Identify the blood parasite species.
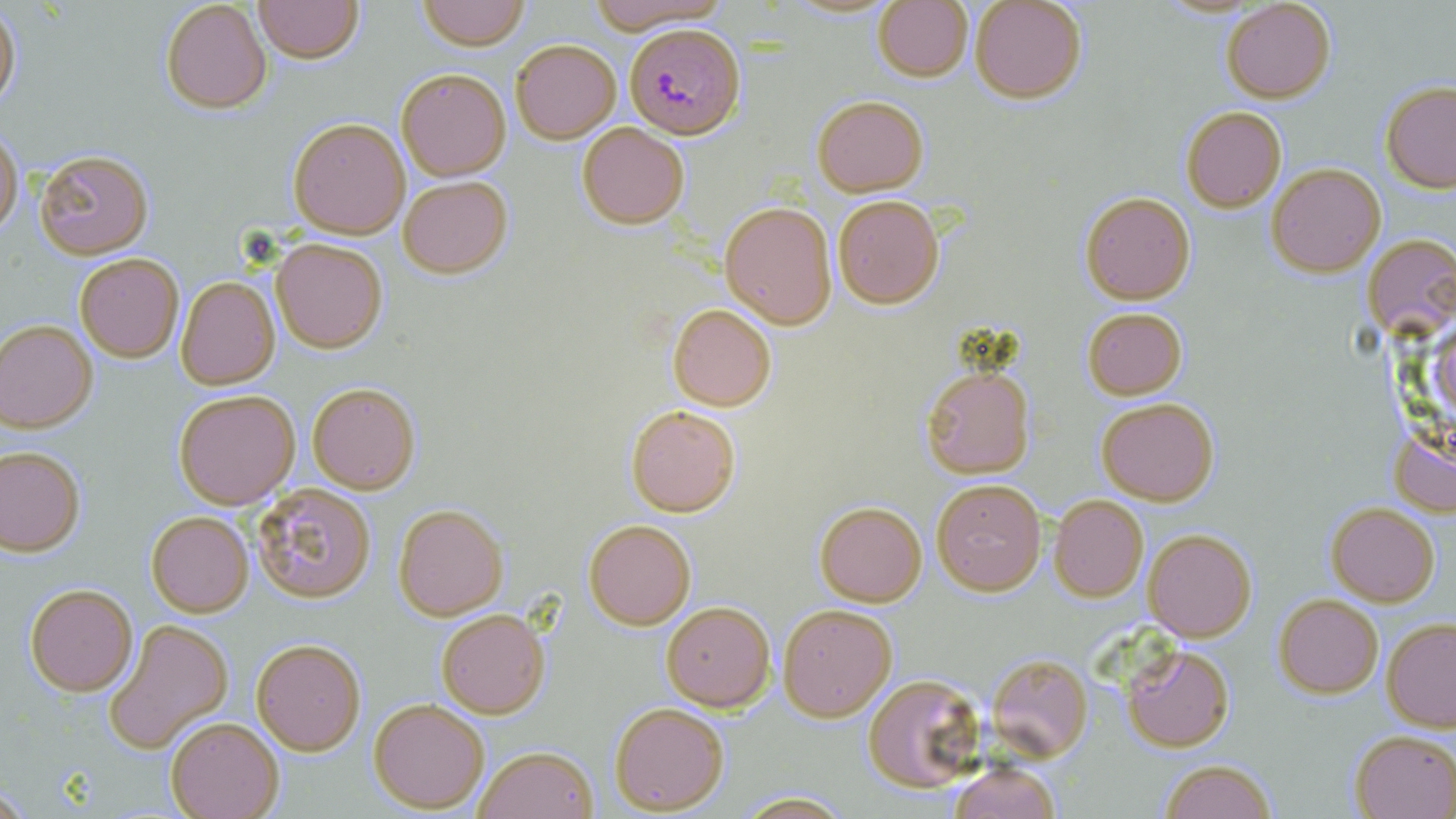
Plasmodium falciparum.

Approximate bounding boxes as (x1,y1)-(x2,y2) corner pairs in pixels. Uninfected red blood cell locations: (253,0)-(363,63), (417,0)-(528,50), (969,0)-(1088,105), (160,1)-(272,114), (582,1)-(731,31), (1220,1)-(1337,104), (872,2)-(974,82), (1,3)-(21,117), (511,39)-(621,144), (395,67)-(511,180), (1380,79)-(1456,193), (810,95)-(928,196), (1180,105)-(1286,213), (288,116)-(410,239), (576,122)-(689,229), (0,127)-(22,239), (33,148)-(155,260), (1267,163)-(1384,277), (397,176)-(512,278), (1079,190)-(1196,305), (834,195)-(944,309), (718,200)-(837,330), (1362,235)-(1454,339), (272,238)-(388,354), (73,253)-(185,363), (70,266)-(280,379), (175,275)-(281,390), (668,303)-(778,412), (1080,307)-(1187,401), (0,319)-(97,432), (920,364)-(1035,478), (307,382)-(421,495), (173,388)-(300,509), (1095,396)-(1220,507), (625,403)-(742,517), (1390,431)-(1456,517), (0,445)-(85,556), (932,478)-(1046,594), (253,482)-(378,603), (1049,495)-(1148,602), (813,499)-(927,606), (1326,502)-(1441,606), (393,503)-(508,620), (145,510)-(254,617), (583,518)-(696,630), (1142,529)-(1257,643), (23,582)-(139,697), (1274,593)-(1384,700), (661,601)-(774,711), (777,602)-(898,722), (436,608)-(550,719), (1382,618)-(1456,731), (103,620)-(234,756), (251,639)-(366,756), (1122,644)-(1233,752), (987,653)-(1093,760), (862,673)-(983,793), (369,697)-(490,812), (608,701)-(730,815), (165,714)-(285,818), (1349,729)-(1456,818), (475,744)-(600,819), (1156,759)-(1279,819), (945,761)-(1062,819), (732,791)-(856,818). Plasmodium falciparum-infected red blood cell locations: (624,21)-(745,138). Thin blood film. 1000x magnification. May-Grünwald-Giemsa stain. Optical microscopy. Single field of view. Image is 1456×819 pixels.